Outline each blood parasite and name the species.
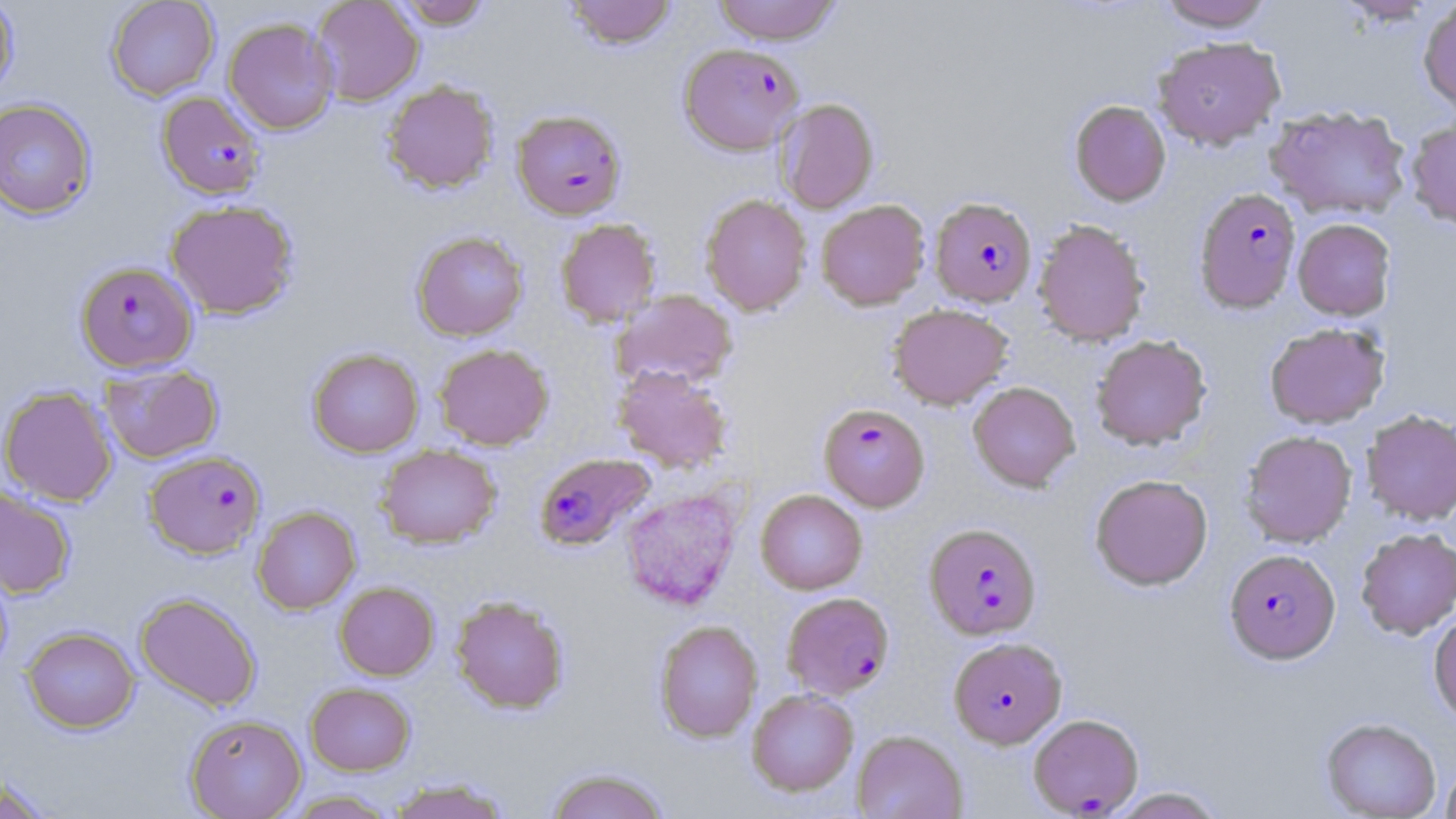

Approximate bounding boxes as named x1/y1/x2/y2 corners in pixels.
Plasmodium falciparum-infected red blood cells: (x1=678, y1=43, x2=803, y2=156), (x1=157, y1=91, x2=266, y2=199), (x1=512, y1=109, x2=626, y2=219), (x1=1193, y1=187, x2=1302, y2=314), (x1=930, y1=197, x2=1037, y2=307), (x1=76, y1=260, x2=197, y2=373), (x1=819, y1=403, x2=930, y2=512), (x1=144, y1=450, x2=266, y2=559), (x1=534, y1=453, x2=655, y2=552), (x1=925, y1=523, x2=1041, y2=640), (x1=1225, y1=549, x2=1340, y2=665), (x1=782, y1=592, x2=895, y2=699), (x1=948, y1=637, x2=1066, y2=748), (x1=1028, y1=713, x2=1144, y2=816).
No Plasmodium ovale, Plasmodium malariae, Plasmodium vivax, Babesia divergens, or Trypanosoma brucei observed.

Uninfected red blood cell locations: (x1=0, y1=0, x2=18, y2=99), (x1=106, y1=0, x2=219, y2=100), (x1=312, y1=0, x2=424, y2=105), (x1=392, y1=0, x2=492, y2=29), (x1=565, y1=0, x2=676, y2=50), (x1=712, y1=0, x2=841, y2=44), (x1=1157, y1=1, x2=1275, y2=31), (x1=1418, y1=1, x2=1456, y2=113), (x1=223, y1=18, x2=338, y2=134), (x1=1152, y1=36, x2=1285, y2=150), (x1=382, y1=80, x2=499, y2=194), (x1=774, y1=98, x2=879, y2=214), (x1=0, y1=99, x2=96, y2=218), (x1=1069, y1=100, x2=1171, y2=207), (x1=1265, y1=106, x2=1412, y2=220), (x1=1405, y1=116, x2=1456, y2=230), (x1=701, y1=194, x2=811, y2=316), (x1=165, y1=199, x2=299, y2=319), (x1=816, y1=200, x2=930, y2=310), (x1=1293, y1=218, x2=1395, y2=320), (x1=556, y1=219, x2=660, y2=327), (x1=1033, y1=220, x2=1149, y2=346), (x1=411, y1=231, x2=528, y2=341), (x1=612, y1=289, x2=738, y2=390), (x1=888, y1=303, x2=1013, y2=409), (x1=1265, y1=323, x2=1389, y2=429), (x1=1091, y1=335, x2=1212, y2=451), (x1=434, y1=343, x2=553, y2=450), (x1=308, y1=348, x2=424, y2=457), (x1=100, y1=364, x2=223, y2=463), (x1=612, y1=366, x2=733, y2=473), (x1=968, y1=382, x2=1080, y2=492), (x1=0, y1=385, x2=118, y2=506), (x1=1362, y1=410, x2=1456, y2=525), (x1=1240, y1=431, x2=1357, y2=548), (x1=376, y1=444, x2=501, y2=548), (x1=1090, y1=474, x2=1213, y2=591), (x1=0, y1=485, x2=76, y2=599), (x1=620, y1=487, x2=743, y2=610), (x1=756, y1=489, x2=867, y2=594), (x1=252, y1=506, x2=360, y2=614), (x1=1356, y1=528, x2=1456, y2=639), (x1=334, y1=582, x2=439, y2=680), (x1=135, y1=592, x2=262, y2=711), (x1=450, y1=595, x2=569, y2=714), (x1=1429, y1=611, x2=1456, y2=724), (x1=654, y1=620, x2=762, y2=742), (x1=21, y1=626, x2=139, y2=733), (x1=305, y1=682, x2=415, y2=775), (x1=747, y1=689, x2=859, y2=796), (x1=185, y1=713, x2=307, y2=818), (x1=1320, y1=717, x2=1441, y2=819), (x1=852, y1=729, x2=968, y2=818), (x1=1440, y1=761, x2=1456, y2=818), (x1=544, y1=767, x2=671, y2=819), (x1=0, y1=775, x2=56, y2=819), (x1=388, y1=778, x2=512, y2=819), (x1=1106, y1=787, x2=1227, y2=818), (x1=281, y1=790, x2=401, y2=818). Slide-level diagnosis: Plasmodium falciparum. May-Grünwald-Giemsa-stained preparation. 1000x magnification. Thin blood film. One field of a larger specimen. Optical microscopy. Image is 1456×819 pixels.